Outline each blood parasite and name the species.
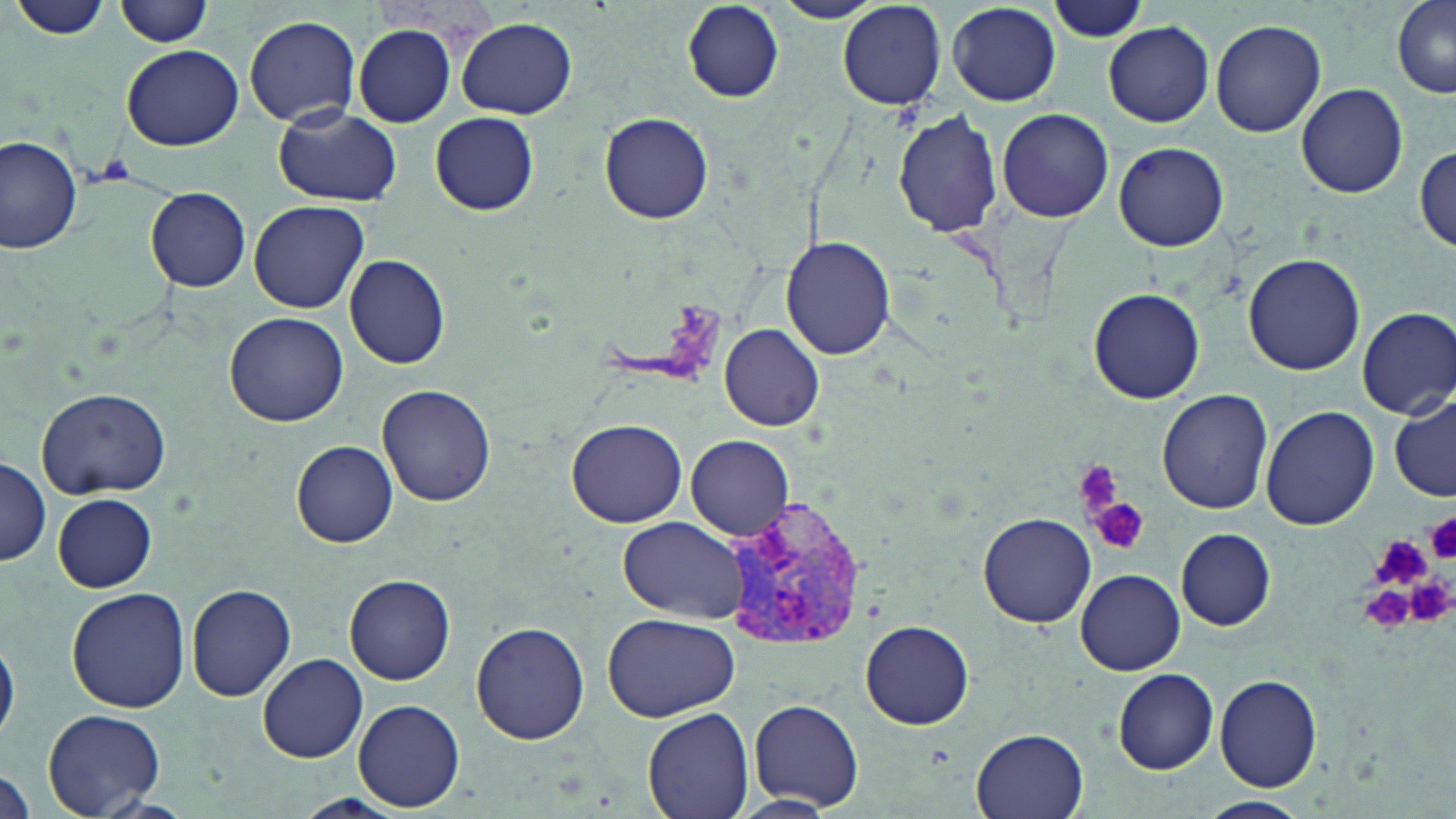

Approximate bounding boxes as [x1, y1, x2, y2] in pixels.
Plasmodium vivax-infected red blood cells: [727, 492, 867, 656].
No Plasmodium falciparum, Plasmodium ovale, Plasmodium malariae, Babesia divergens, or Trypanosoma brucei observed.

slide-level diagnosis = Plasmodium vivax
field of view = single
preparation = thin blood film
platelet locations = approximate bounding boxes as [x1, y1, x2, y2] in pixels: [1069, 459, 1125, 521], [1091, 498, 1147, 556], [1424, 513, 1456, 563], [1373, 540, 1431, 583], [1406, 573, 1455, 626], [1353, 580, 1424, 633]
stain = May-Grünwald-Giemsa
uninfected red blood cell locations = approximate bounding boxes as [x1, y1, x2, y2] in pixels: [771, 0, 888, 25], [115, 1, 213, 48], [1050, 1, 1152, 43], [1390, 1, 1456, 101], [12, 2, 114, 42], [837, 2, 947, 109], [681, 3, 783, 102], [948, 3, 1064, 105], [244, 14, 361, 126], [457, 18, 576, 119], [1210, 19, 1325, 137], [1104, 21, 1213, 127], [353, 24, 456, 127], [122, 44, 244, 150], [1296, 83, 1408, 199], [272, 107, 401, 206], [997, 108, 1114, 223], [599, 110, 713, 224], [429, 111, 540, 215], [895, 111, 1002, 238], [1, 134, 81, 253], [1113, 141, 1230, 252], [1414, 146, 1454, 253], [145, 187, 251, 291], [248, 200, 370, 313], [780, 236, 896, 358], [1243, 251, 1364, 375], [344, 253, 449, 369], [1086, 287, 1206, 403], [1356, 306, 1456, 419], [225, 311, 348, 426], [719, 324, 824, 432], [376, 386, 496, 506], [36, 388, 170, 499], [1157, 388, 1273, 514], [1390, 393, 1455, 501], [1259, 407, 1380, 532], [566, 418, 686, 528], [686, 435, 794, 540], [290, 440, 398, 547], [0, 456, 51, 567], [53, 494, 156, 592], [979, 511, 1096, 627], [618, 516, 748, 622], [1176, 528, 1276, 630], [1075, 568, 1185, 674], [344, 575, 456, 685], [187, 584, 296, 700], [68, 587, 192, 714], [602, 612, 738, 722], [861, 620, 975, 730], [471, 622, 590, 744], [0, 631, 19, 744], [259, 653, 369, 763], [1114, 669, 1218, 774], [1215, 674, 1322, 791], [354, 699, 464, 811], [750, 699, 863, 811], [643, 706, 753, 819], [45, 710, 164, 815], [968, 727, 1092, 819], [0, 766, 36, 817], [731, 794, 839, 817], [292, 795, 411, 819], [1196, 795, 1311, 818]
modality = optical microscopy
magnification = 1000x
image size = 1456×819 pixels